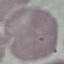
Malaria status: uninfected. Giemsa stain. Acquired by smartphone through the microscope eyepiece. Thin smear of blood. Cell patch, automatically extracted from a larger field of view and resized to 64 × 64 pixels.